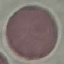 Result: no malaria parasites seen. Giemsa-stained preparation. Thin smear of blood. Automatically extracted cell patch, resized to 64 × 64 pixels. Photographed with a smartphone camera at the microscope eyepiece.